Report the malaria status.
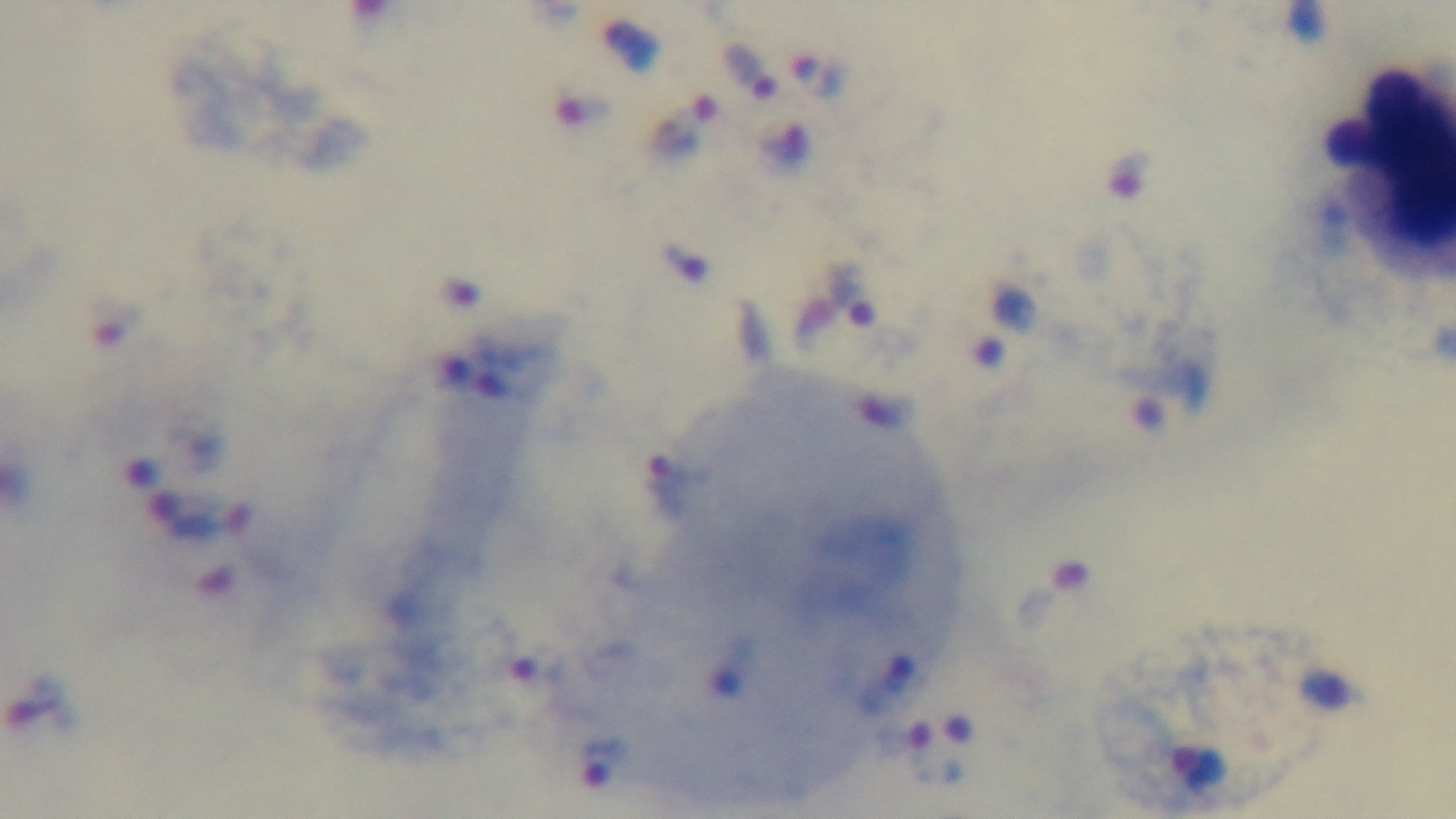
Infected.

{
  "preparation": "thick smear",
  "field_of_view": "single",
  "capture": "mounted 4K digital camera",
  "stain": "Giemsa",
  "objective": "100x oil immersion",
  "modality": "light microscopy"
}